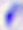
identification = Toxoplasma gondii
modality = photomicrograph
magnification = 400x